Locate every Trypanosoma brucei.
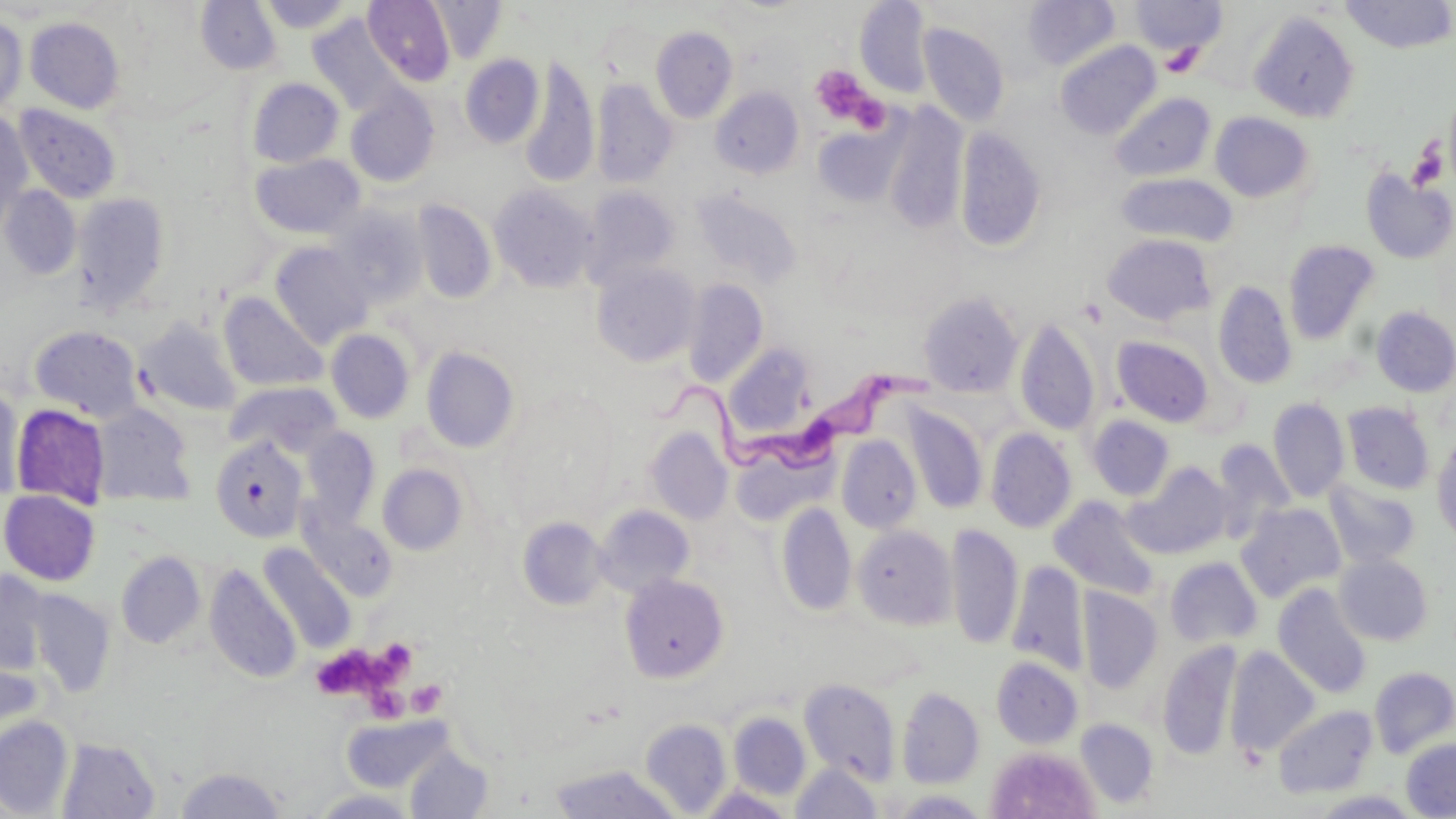

Approximate bounding boxes as [x1, y1, x2, y2] in pixels.
Trypanosoma brucei: [641, 359, 936, 478].

Summary:
  - Platelet locations: [1160, 44, 1204, 77], [810, 65, 881, 129], [1409, 141, 1448, 190], [375, 639, 416, 680], [318, 647, 381, 699], [407, 680, 447, 717], [366, 683, 413, 729]
  - Uninfected red blood cell locations: [258, 0, 354, 32], [363, 0, 455, 85], [429, 0, 506, 62], [855, 0, 933, 98], [1023, 0, 1120, 70], [1130, 0, 1228, 58], [195, 1, 281, 75], [1340, 1, 1456, 53], [1249, 11, 1360, 123], [308, 14, 404, 115], [0, 15, 27, 114], [25, 17, 124, 113], [918, 23, 1010, 127], [650, 26, 737, 123], [1055, 40, 1161, 140], [460, 54, 544, 148], [520, 57, 599, 188], [247, 78, 344, 168], [592, 79, 677, 189], [346, 86, 440, 187], [711, 86, 804, 179], [1109, 92, 1216, 182], [14, 104, 122, 204], [881, 104, 969, 235], [0, 112, 33, 222], [1210, 112, 1314, 203], [812, 123, 905, 207], [954, 127, 1046, 253], [251, 153, 365, 240], [1361, 169, 1456, 264], [1116, 172, 1237, 247], [1, 185, 82, 281], [490, 185, 598, 293], [582, 186, 680, 288], [691, 189, 802, 288], [72, 191, 171, 314], [412, 199, 497, 305], [326, 207, 426, 308], [1102, 233, 1217, 326], [1282, 239, 1380, 344], [270, 242, 372, 347], [591, 262, 701, 367], [683, 279, 768, 388], [1213, 280, 1297, 390], [918, 291, 1024, 398], [218, 292, 327, 393], [1372, 305, 1456, 397], [136, 317, 242, 416], [1015, 317, 1101, 436], [29, 325, 143, 421], [325, 328, 415, 424], [1112, 336, 1214, 427], [723, 344, 814, 439], [421, 347, 518, 452], [226, 382, 341, 457], [1, 387, 25, 502], [1267, 397, 1349, 503], [1342, 401, 1435, 495], [10, 403, 111, 508], [91, 404, 195, 507], [903, 404, 988, 514], [1086, 415, 1175, 501], [301, 426, 380, 524], [645, 428, 733, 524], [985, 428, 1077, 533], [1432, 434, 1456, 546], [836, 435, 921, 533], [211, 436, 307, 543], [1212, 438, 1295, 536], [1125, 462, 1233, 559], [377, 463, 468, 556], [1323, 480, 1421, 569], [1, 489, 100, 585], [1049, 495, 1160, 599], [776, 502, 856, 616], [1236, 502, 1346, 603], [594, 505, 695, 597], [301, 511, 396, 600], [517, 516, 609, 610], [945, 523, 1023, 651], [853, 525, 956, 630], [258, 544, 357, 653], [115, 550, 206, 649], [1335, 554, 1434, 646], [1165, 557, 1262, 647], [1007, 562, 1089, 675], [204, 564, 302, 683], [0, 569, 51, 675], [619, 573, 729, 682], [1273, 583, 1372, 698], [1079, 589, 1163, 694], [27, 590, 116, 695], [1156, 640, 1241, 761], [1225, 646, 1320, 758], [991, 656, 1082, 748], [1369, 666, 1456, 758], [800, 677, 900, 784], [897, 686, 984, 788], [1273, 704, 1378, 799], [728, 712, 810, 800], [343, 714, 455, 793], [0, 715, 74, 817], [1075, 717, 1159, 808], [640, 719, 731, 816], [57, 737, 161, 818], [1400, 737, 1456, 817], [405, 745, 494, 818], [986, 746, 1100, 819], [791, 762, 883, 818], [549, 763, 680, 819], [174, 766, 287, 818], [309, 789, 420, 818], [890, 790, 992, 818]
  - Slide-level diagnosis: Trypanosoma brucei
  - Stain: May-Grünwald-Giemsa
  - Preparation: thin blood film
  - Field of view: one of a larger specimen
  - Magnification: 1000x
  - Image size: 1456×819 pixels
  - Modality: optical microscopy